Identify the preparation type.
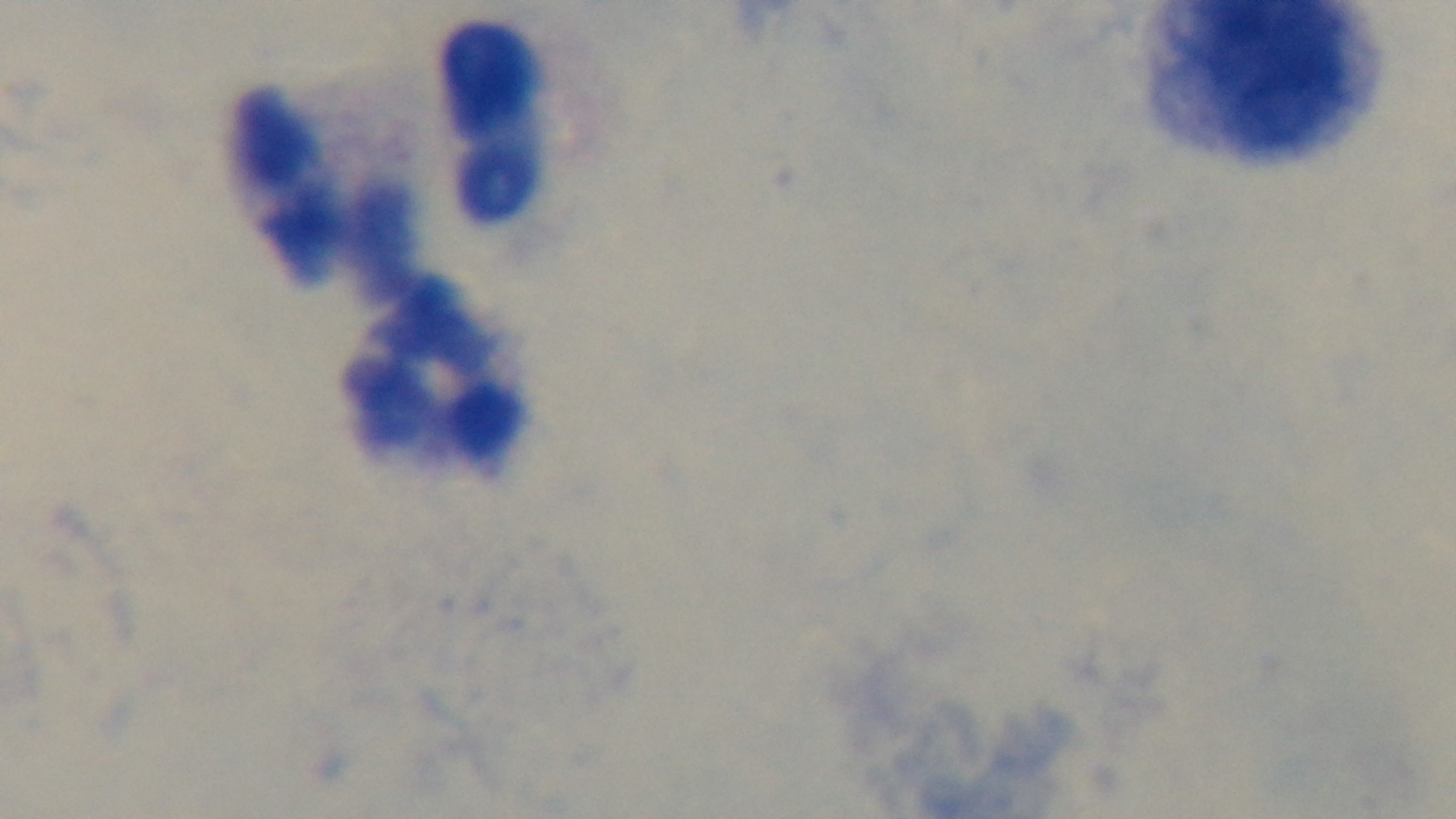
Thick.

Giemsa-stained. Malaria status: uninfected. Single field of view. Photomicrograph. Oil-immersion objective, 100x. Captured with a mounted 4K digital camera.